Identify the parasite.
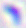
Toxoplasma gondii.

Summary:
  - Magnification: 400x
  - Modality: photomicrograph